Give the position of every Plasmodium parasite.
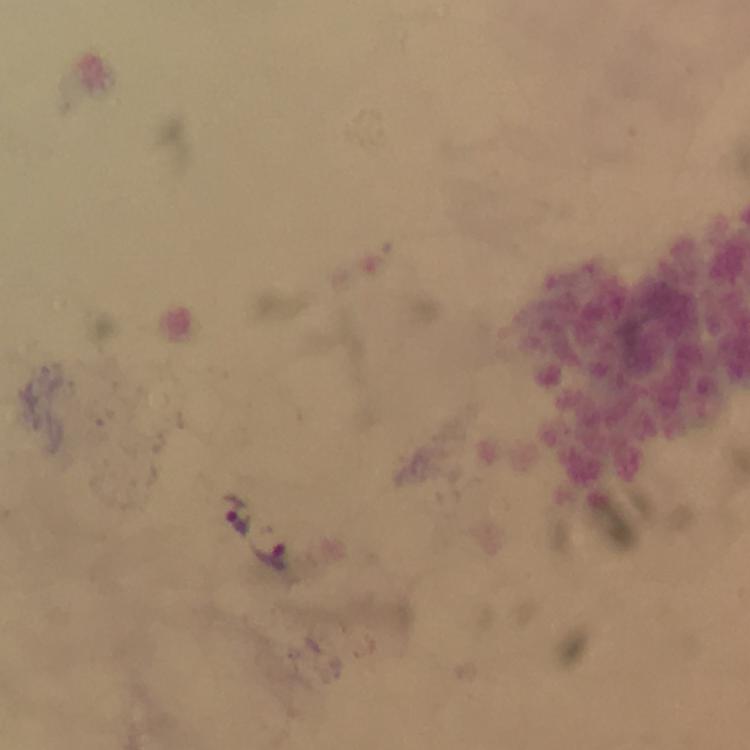
Approximate object centers, in pixels from the top-left corner.
Plasmodium parasites: (x=238, y=514), (x=270, y=558).

Photographed through the microscope with a smartphone camera. At 100x magnification. Immersion oil applied. From a malaria diagnostic workup. Image is 750×750 pixels. Giemsa stain. A crop from one field of view. Thick blood smear.